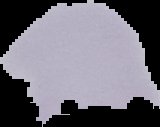 Cell region segmented out of the field of view; the surrounding area is masked to black. Image is 160×127 pixels. Malaria status: uninfected. From a thin blood smear.